Report the malaria status of this cell.
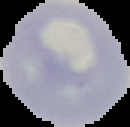
It is uninfected.

Image is 130×127 pixels. From a thin blood film. The area outside the segmented cell region is set to black.